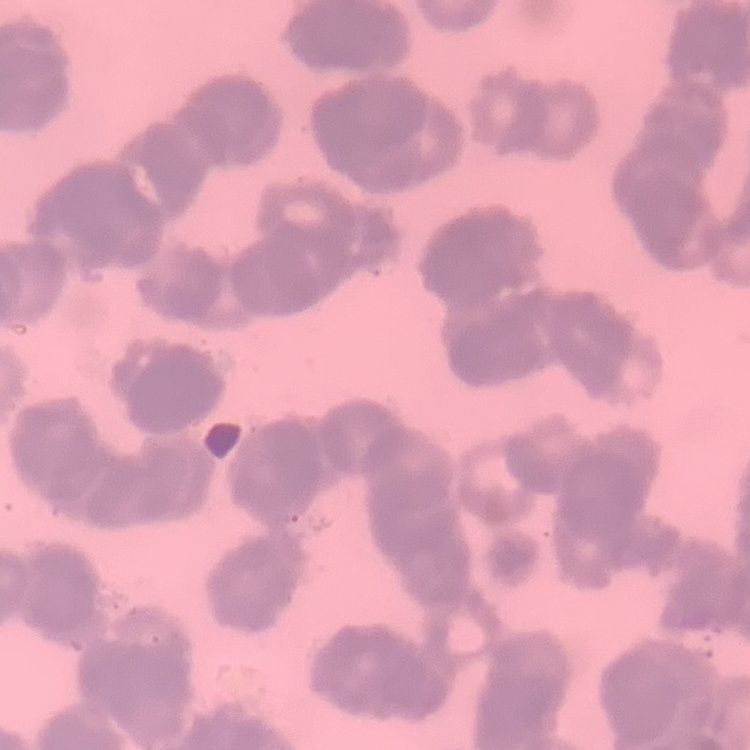
erythrocyte_morphology: rouleaux formation
image_type: one tile cut from a larger photomicrograph
preparation: thin peripheral smear
stain: Field's or Giemsa